Report the malaria status of this cell.
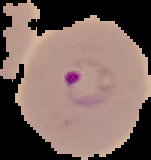

It is parasitized.

Summary:
  - Preparation: thin blood smear
  - Image type: segmented cell region on a black background
  - Image size: 151×160 pixels